Outline every malaria parasite.
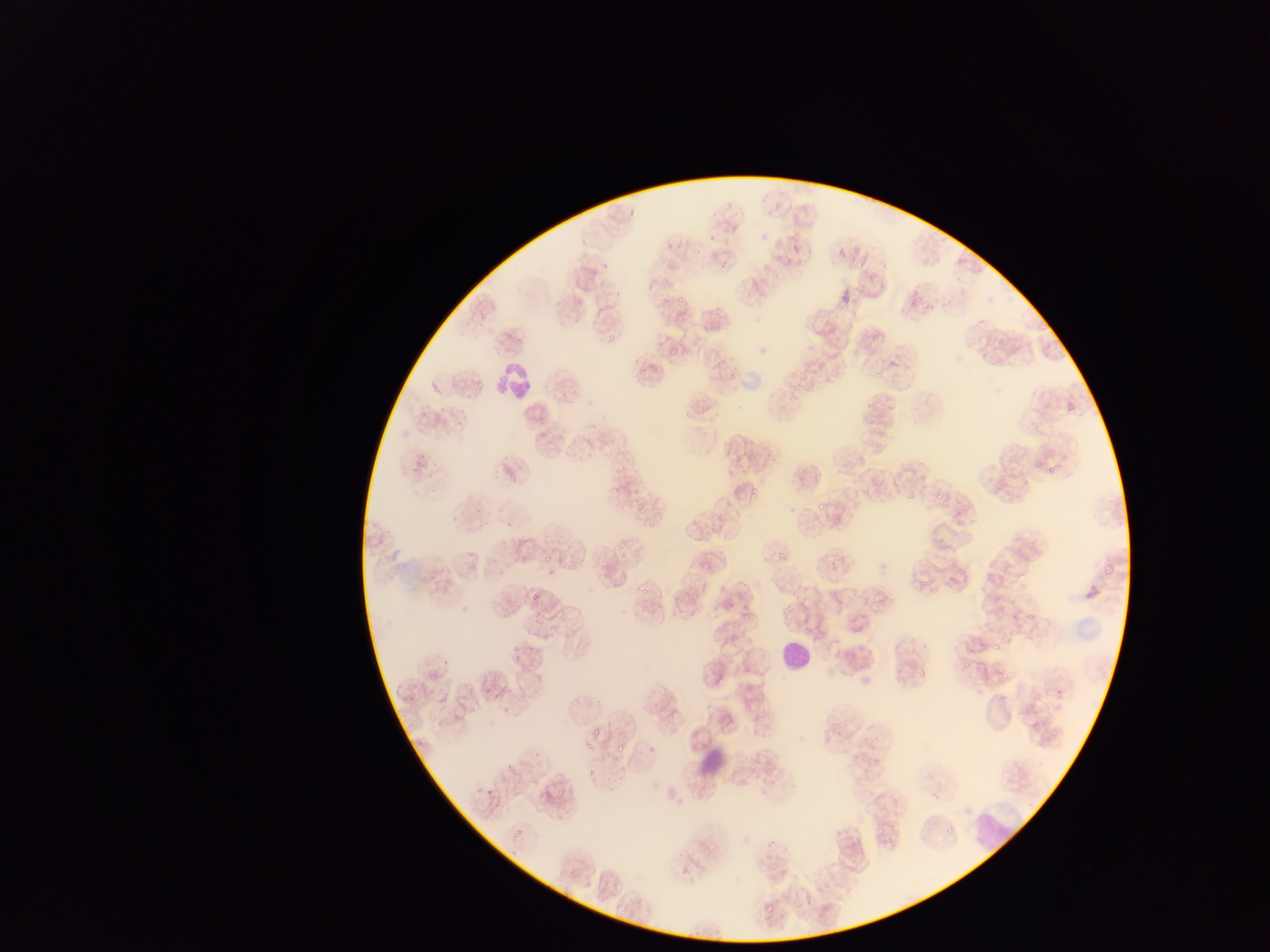

Approximate bounding boxes as {left, top, right, bottom} in pixels.
Malaria parasites: {762, 263, 771, 269}, {677, 293, 689, 303}, {608, 334, 617, 343}, {671, 344, 678, 352}, {714, 359, 723, 368}, {830, 364, 842, 374}, {726, 369, 740, 379}, {1060, 395, 1084, 420}, {624, 444, 633, 453}, {1005, 453, 1016, 462}, {1045, 464, 1054, 473}, {990, 485, 998, 492}, {751, 487, 760, 494}, {636, 491, 644, 514}, {905, 492, 913, 500}, {844, 509, 852, 519}, {689, 514, 699, 524}, {646, 521, 655, 529}, {778, 547, 788, 560}, {544, 555, 553, 562}, {818, 557, 825, 565}, {688, 561, 696, 569}, {563, 562, 572, 572}, {917, 575, 931, 590}, {639, 584, 649, 598}, {530, 590, 544, 605}, {843, 611, 869, 639}, {778, 612, 787, 620}, {1026, 612, 1038, 621}, {560, 613, 567, 622}, {991, 636, 1005, 649}, {512, 644, 520, 653}, {440, 655, 449, 664}, {532, 662, 538, 670}, {664, 683, 672, 693}, {486, 686, 494, 695}, {502, 702, 510, 714}, {651, 707, 660, 713}, {590, 725, 597, 737}, {750, 725, 759, 737}, {577, 739, 593, 753}, {613, 742, 625, 752}, {647, 743, 657, 753}, {584, 767, 592, 776}, {531, 774, 539, 784}, {680, 785, 696, 794}, {568, 786, 577, 795}, {484, 788, 493, 797}, {544, 789, 558, 799}, {944, 824, 953, 834}, {511, 825, 527, 837}, {766, 834, 780, 849}, {766, 898, 780, 913} | approximate {x, y} pixel centers of objects too small to bound: {478, 383}, {418, 463}, {625, 477}, {623, 487}, {938, 497}, {820, 505}, {835, 521}, {805, 524}, {549, 571}, {681, 582}, {523, 666}, {966, 666}, {920, 673}, {472, 704}.

leukocyte locations = approximate bounding boxes as {left, top, right, bottom} in pixels: {489, 361, 530, 397}, {773, 631, 822, 681}, {970, 801, 1007, 847}
artifact (stain precipitate or debris) locations = approximate bounding boxes as {left, top, right, bottom} in pixels: {690, 740, 730, 783}
capture = mobile-phone photograph through a microscope
field of view = single
image size = 1270×952 pixels
preparation = thin blood film
country = Ghana